Locate every Plasmodium vivax-infected red blood cell.
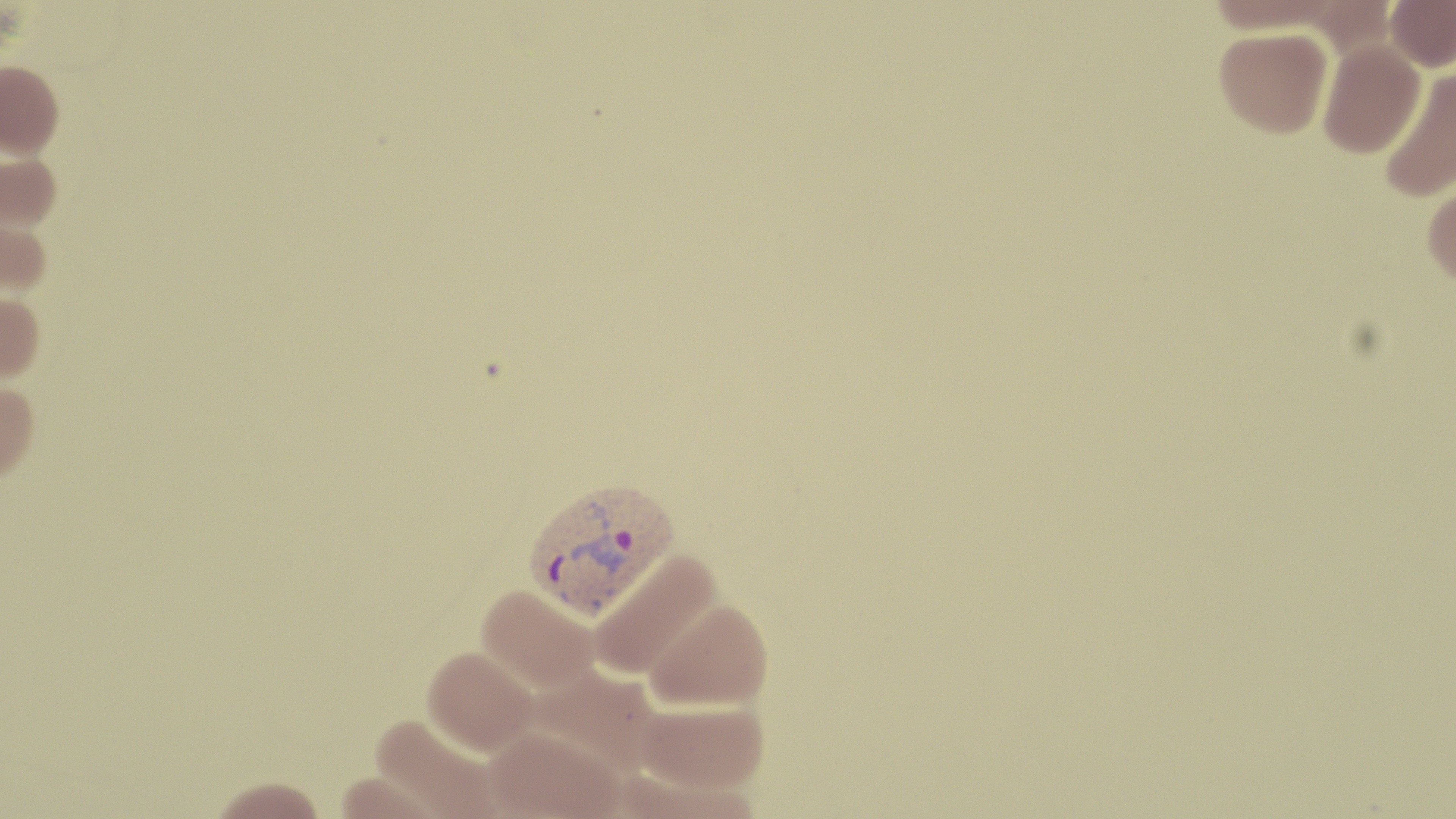

Approximate bounding boxes as (x1, y1, x2, y2) in pixels.
Plasmodium vivax-infected red blood cells: (523, 476, 681, 621).

Summary:
  - Uninfected red blood cell locations: (1206, 0, 1346, 35), (1385, 0, 1456, 72), (1214, 26, 1332, 137), (1317, 38, 1425, 157), (0, 62, 63, 158), (1379, 65, 1456, 202), (0, 150, 62, 232), (1422, 178, 1456, 292), (0, 215, 52, 297), (0, 292, 45, 382), (0, 381, 39, 485), (588, 549, 724, 681), (476, 584, 601, 695), (644, 598, 773, 711), (423, 645, 539, 756), (634, 699, 770, 794), (369, 714, 505, 819), (485, 726, 623, 819), (207, 778, 328, 819)
  - Slide-level diagnosis: Plasmodium vivax
  - Image size: 1456×819 pixels
  - Magnification: 1000x
  - Modality: light microscopy
  - Field of view: single
  - Stain: May-Grünwald-Giemsa
  - Preparation: thin blood smear